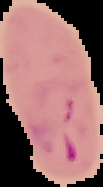
image type = segmented cell region with the area outside set to black
image size = 103×187 pixels
result = Plasmodium parasites identified
preparation = thin blood smear